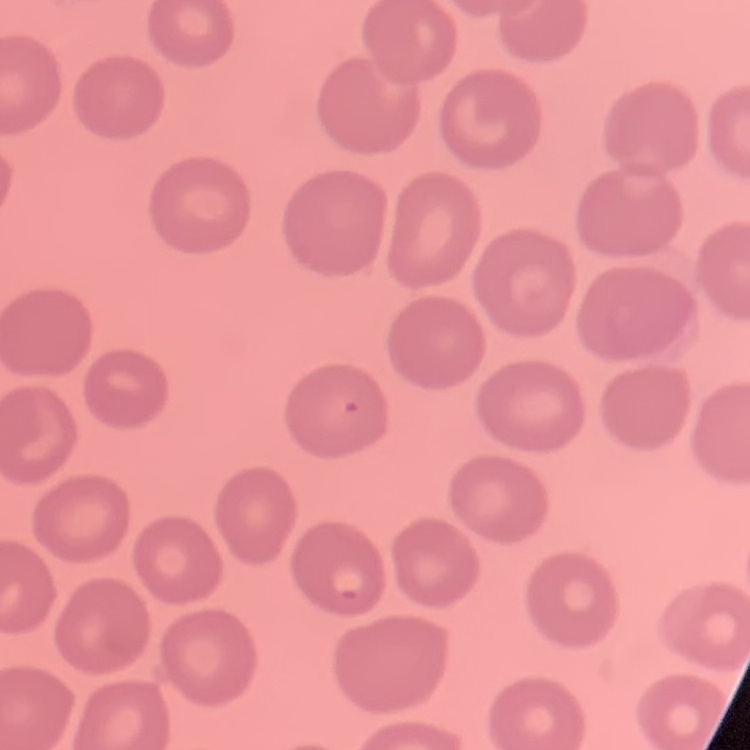
erythrocyte morphology = no rouleaux formation
preparation = thin blood smear
stain = Field's or Giemsa
image type = square crop of a larger photomicrograph